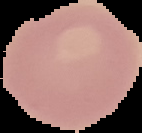
Summary:
  - Preparation: thin blood smear
  - Image type: cell region segmented out of the field of view; surrounding area masked to black
  - Image size: 142×133 pixels
  - Malaria status: uninfected